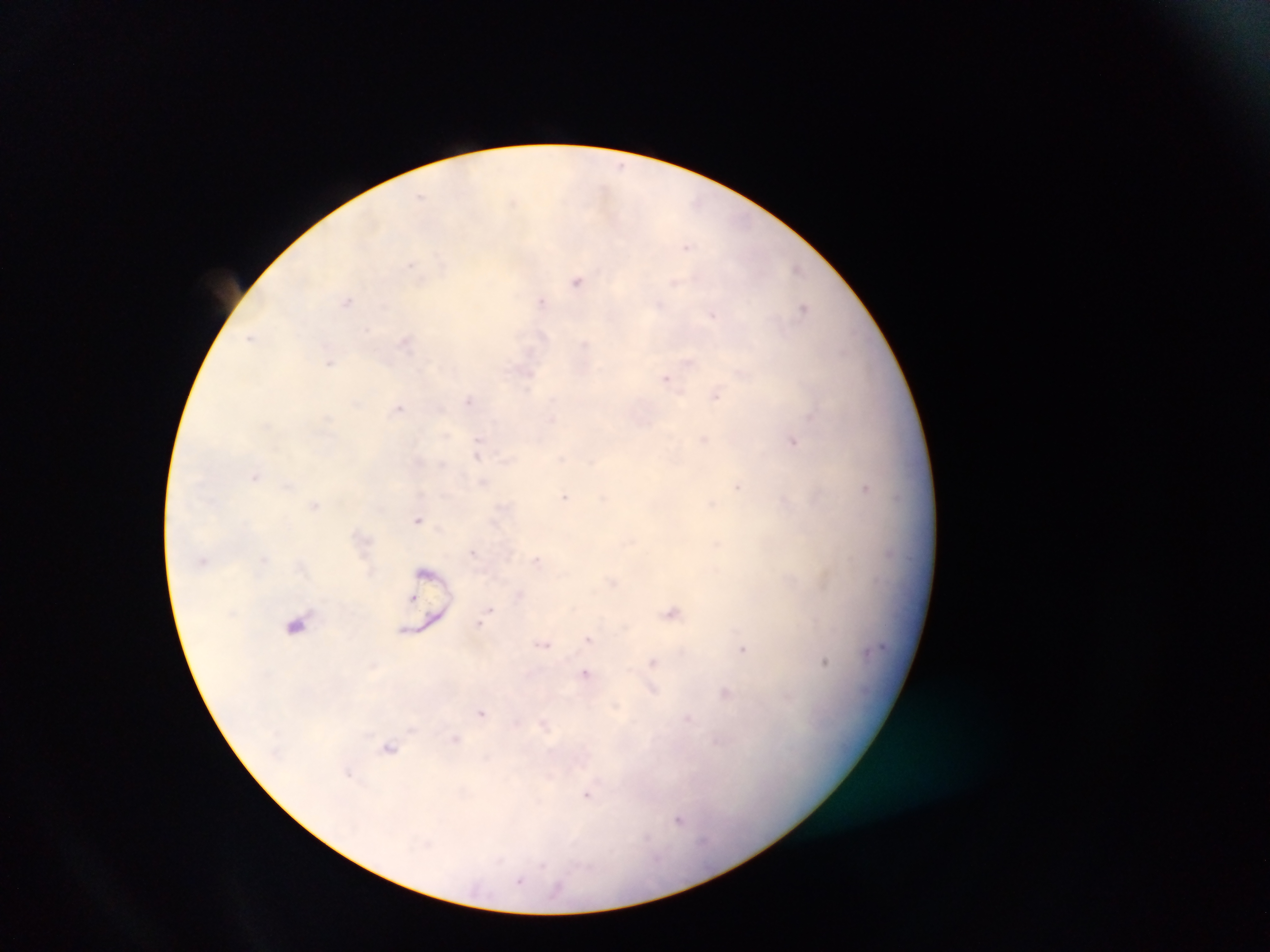

Plasmodium parasite locations = approximate centers as [x, y] in pixels: [620, 165], [420, 196], [687, 248], [411, 264], [796, 269], [577, 281], [675, 282], [540, 300], [348, 301], [659, 304], [803, 308], [713, 315], [366, 329], [251, 337], [405, 341], [329, 362], [529, 376], [666, 379], [716, 395], [469, 400], [398, 408], [704, 439], [793, 442], [478, 444], [477, 453], [255, 476], [738, 486], [865, 488], [565, 496], [711, 504], [315, 505], [418, 520], [537, 559], [612, 583], [490, 610], [671, 612], [480, 624], [588, 638], [544, 644], [743, 649], [653, 662], [824, 662], [585, 674], [725, 694], [481, 713], [687, 719], [455, 740], [389, 748], [349, 772], [586, 795], [679, 820], [520, 880]
field of view = single
image size = 1270×952 pixels
preparation = thick blood smear
country = Ghana
capture = mobile-phone photograph through a microscope